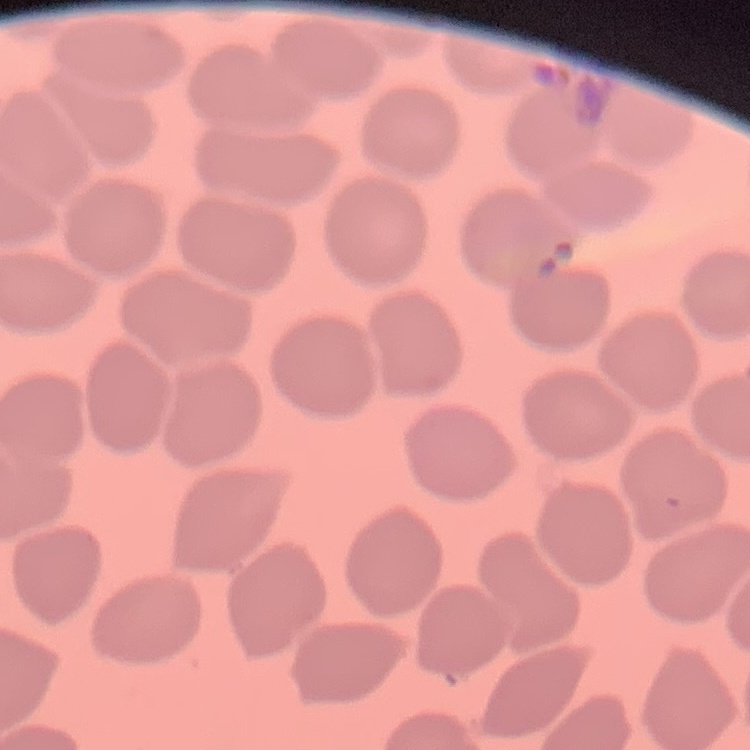
Summary:
  - Red blood cell morphology: no rouleaux formation
  - Preparation: thin peripheral smear
  - Image type: one tile cut from a larger photomicrograph
  - Stain: Field's or Giemsa